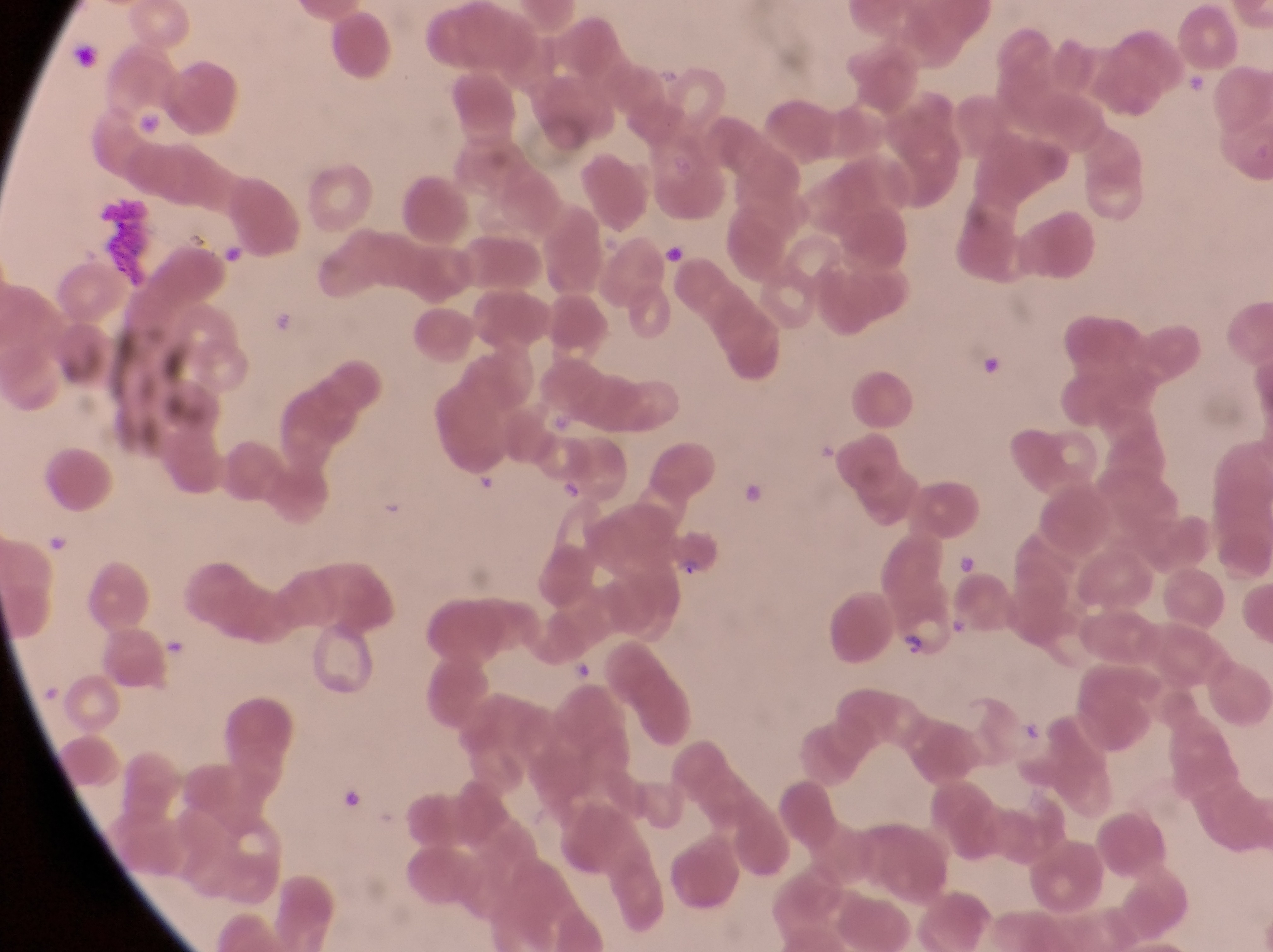 Approximate bounding boxes as left top right bottom in pixels. Leukocyte locations: 92 197 157 281. Parasitised red blood cell locations: 669 535 721 580; 891 605 960 667. Artifact (platelet-like body, stain precipitate, or debris) locations: 217 239 250 269; 663 240 686 272; 978 344 1005 381; 473 473 502 499; 744 478 768 506; 42 529 73 558; 341 789 364 817. Captured by a smartphone held over the eyepiece of an Olympus CX-23 microscope. Sample from Uganda. Thin blood film. Single field of view. Magnification of 1000x. Image is 1273×952 pixels.